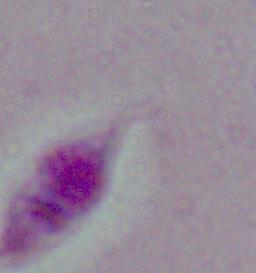

magnification = 1000x
modality = photomicrograph
identification = Leishmania